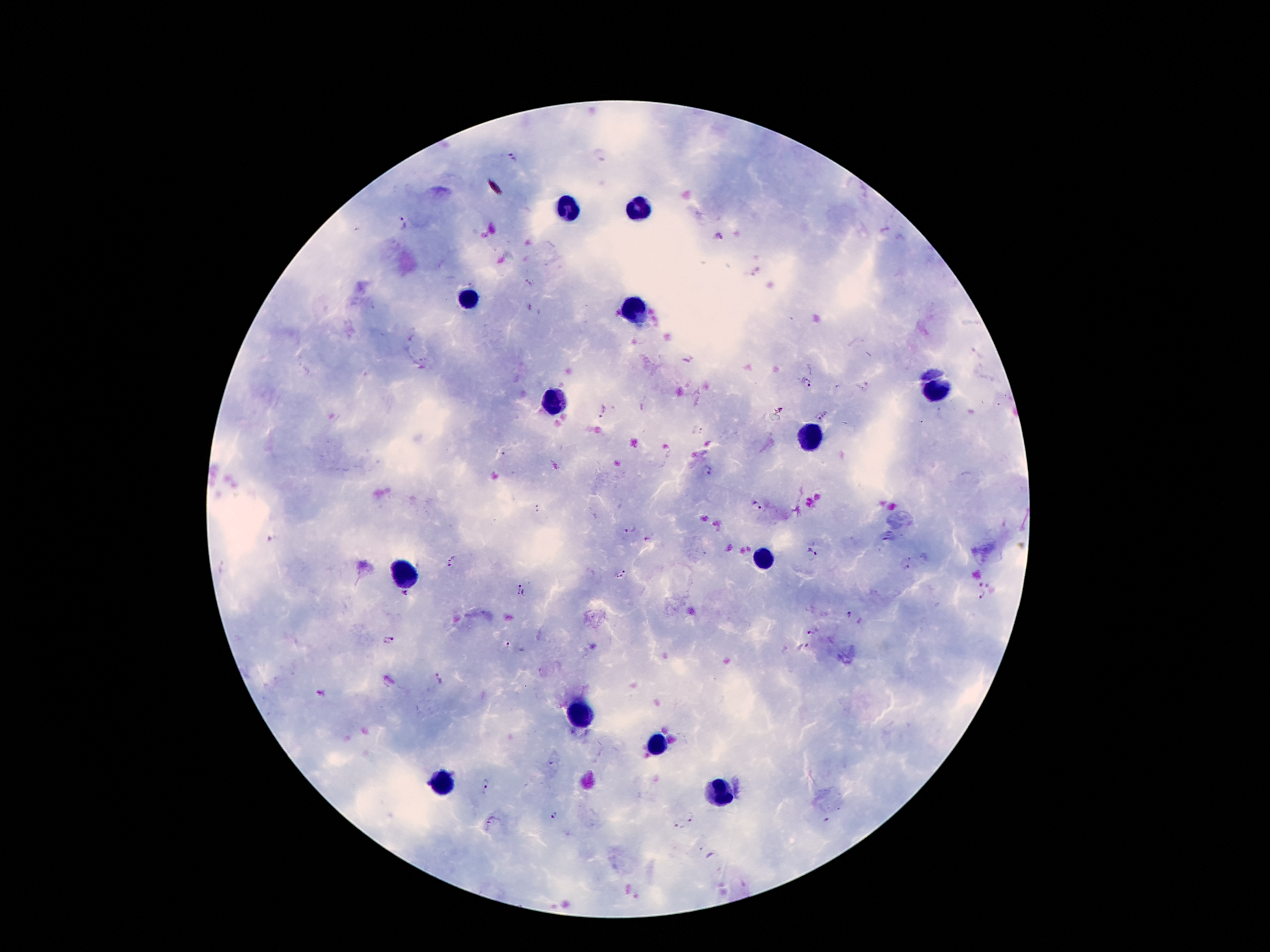

Approximate centers as {x, y} in pixels. Plasmodium parasite locations: {513, 157}, {403, 224}, {718, 235}, {806, 382}, {602, 411}, {820, 418}, {697, 430}, {708, 470}, {757, 507}, {628, 529}, {813, 551}, {449, 564}, {905, 565}, {625, 570}, {619, 577}, {978, 585}, {990, 586}, {521, 590}, {983, 597}, {848, 614}, {812, 632}, {389, 641}, {508, 646}, {804, 647}, {437, 680}, {553, 765}, {487, 784}, {553, 816}, {691, 817}, {492, 819}, {826, 821}, {678, 825}. Leukocyte locations: {571, 208}, {638, 208}, {466, 301}, {638, 306}, {935, 393}, {555, 401}, {811, 438}, {764, 559}, {408, 577}, {579, 715}, {656, 744}, {445, 782}, {716, 793}. Smartphone photograph taken through the microscope eyepiece. Patient malaria status: positive for Plasmodium falciparum. Thick peripheral-blood smear. Single field of view. Giemsa-stained preparation. Image is 1270×952 pixels. 100x magnification.